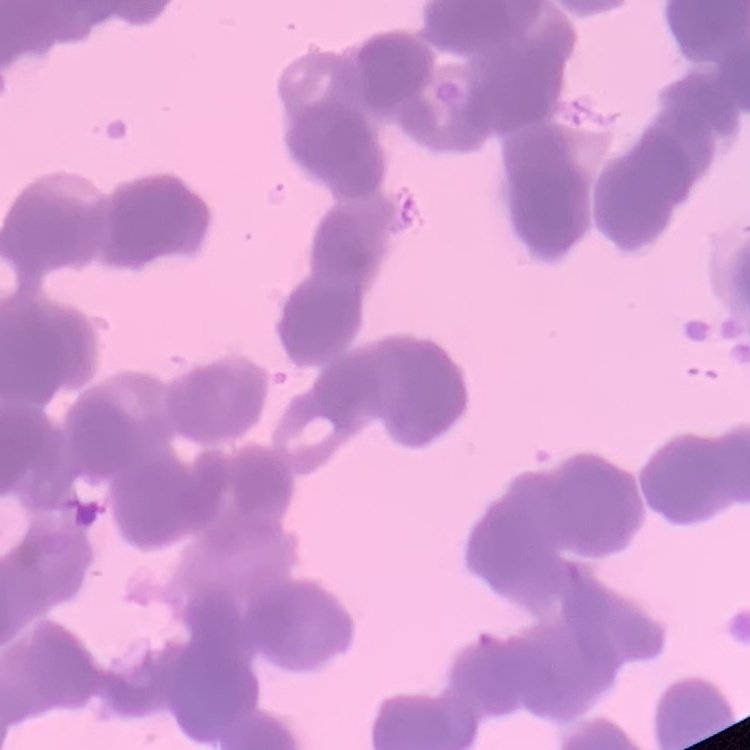 The erythrocytes exhibit rouleaux formation. Thin peripheral smear. Stained with either Field's or Giemsa. One tile cut from a larger photomicrograph.